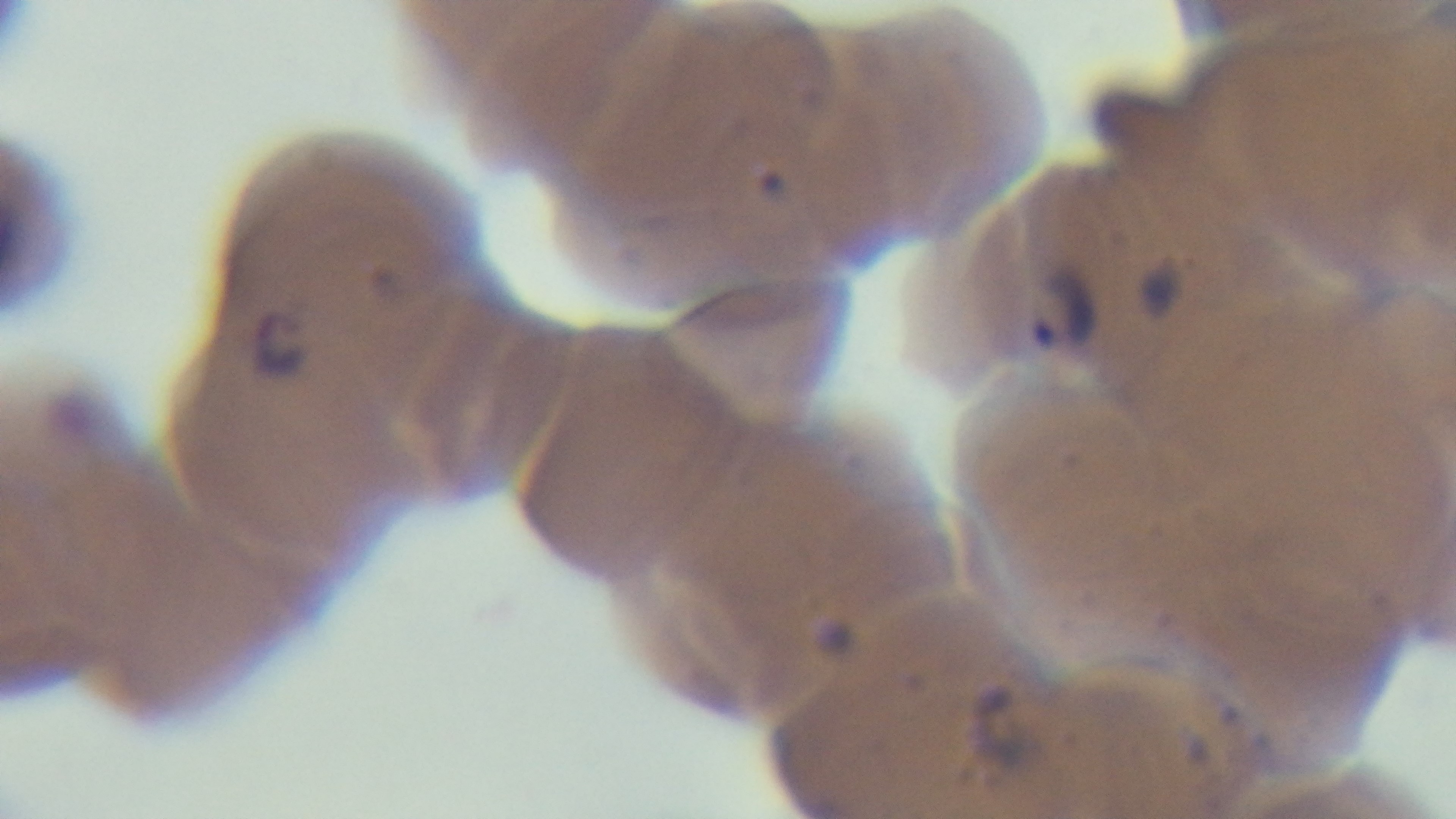

field_of_view: one from the slide
malaria_status: positive
capture: mounted 4K digital camera
modality: light microscopy
objective: 100x oil immersion
stain: Giemsa
preparation: thin smear